Describe the morphology of the erythrocytes.
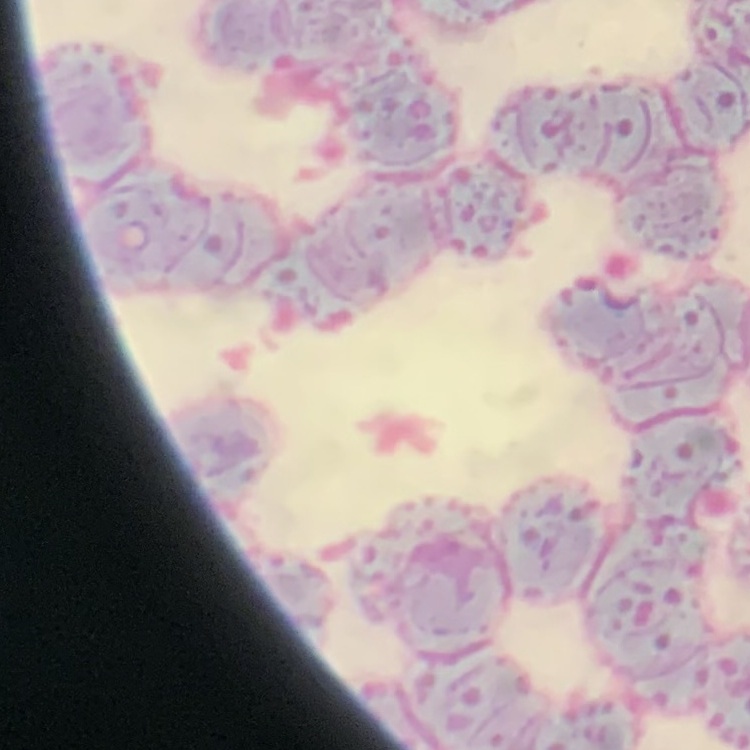
They show rouleaux formation.

Summary:
  - Image type: square crop of a larger photomicrograph
  - Preparation: thin blood film
  - Stain: Field's or Giemsa